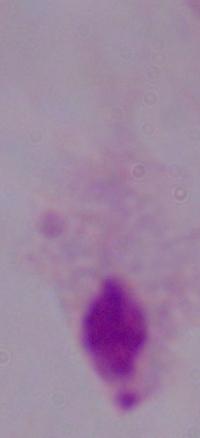

A trichomonad is shown. 1000x magnification. Photomicrograph.